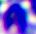
identification: leukocyte
magnification: 400x
modality: photomicrograph